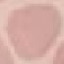
malaria status = uninfected
stain = Giemsa
capture = smartphone through the microscope eyepiece
preparation = thin smear
image type = automatically extracted cell patch, resized to 64 × 64 pixels